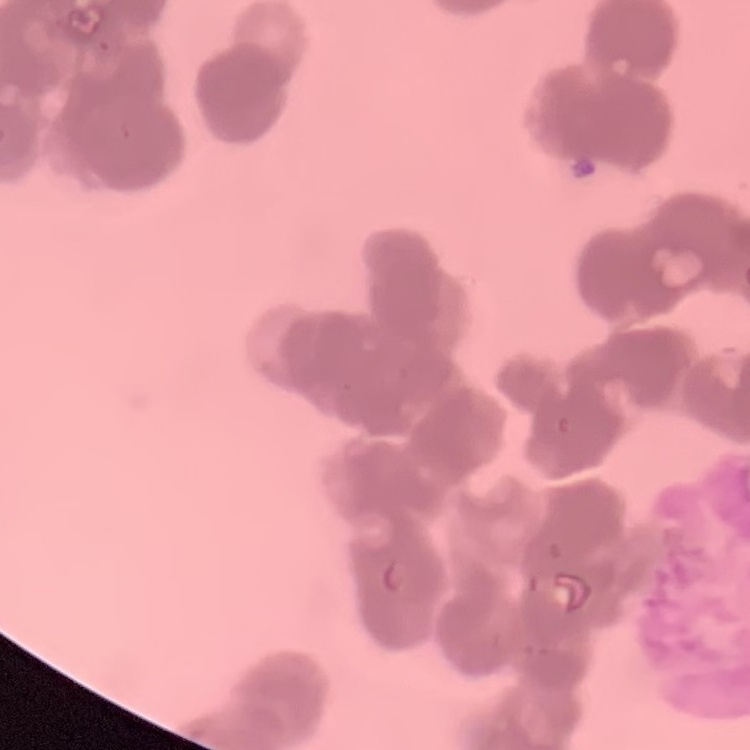
The red blood cells exhibit rouleaux formation. One tile cut from a larger photomicrograph. Stained with either Field's or Giemsa. Thin peripheral smear.